Describe the morphology of the red blood cells.
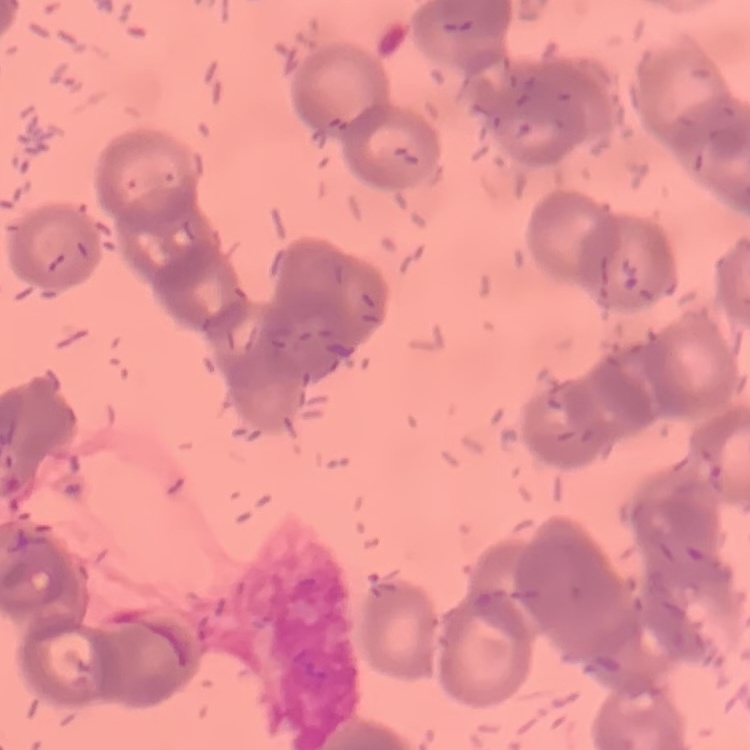

They show rouleaux formation.

stain = Field's or Giemsa
preparation = thin blood smear
image type = one tile cut from a larger photomicrograph